Give the preparation type.
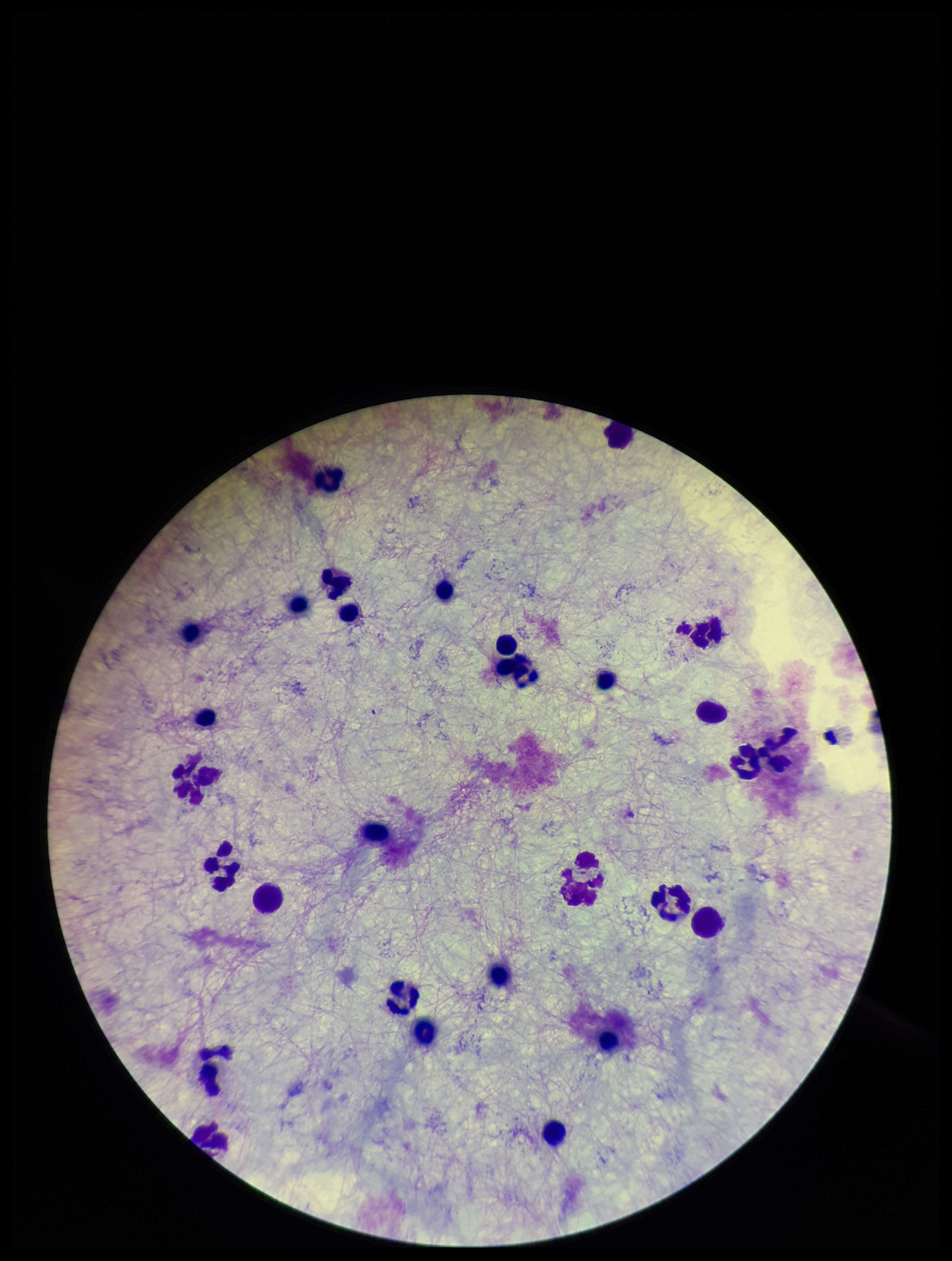

Thick.

{
  "leukocyte_count": 30,
  "plasmodium_parasites": "none identified",
  "capture": "smartphone photograph through the microscope eyepiece",
  "image_size": "952×1261 pixels",
  "patient_malaria_status": "negative",
  "stain": "Giemsa",
  "parasite_count": 0,
  "field_of_view": "single"
}